Classify this cell by malaria status.
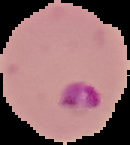
It is parasitized.

Summary:
  - Preparation: thin blood smear
  - Image size: 130×145 pixels
  - Image type: cell region segmented out of the field of view; surrounding area masked to black